Report the malaria status of this cell.
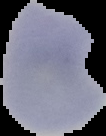
It is parasitized.

image type = segmented cell region on a black background
image size = 106×136 pixels
preparation = thin blood film